State which parasite is depicted.
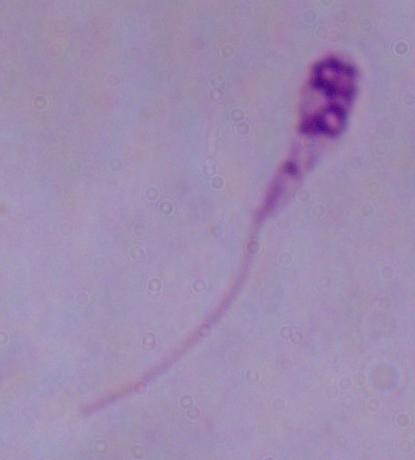

Leishmania.

{
  "modality": "micrograph",
  "magnification": "1000x"
}